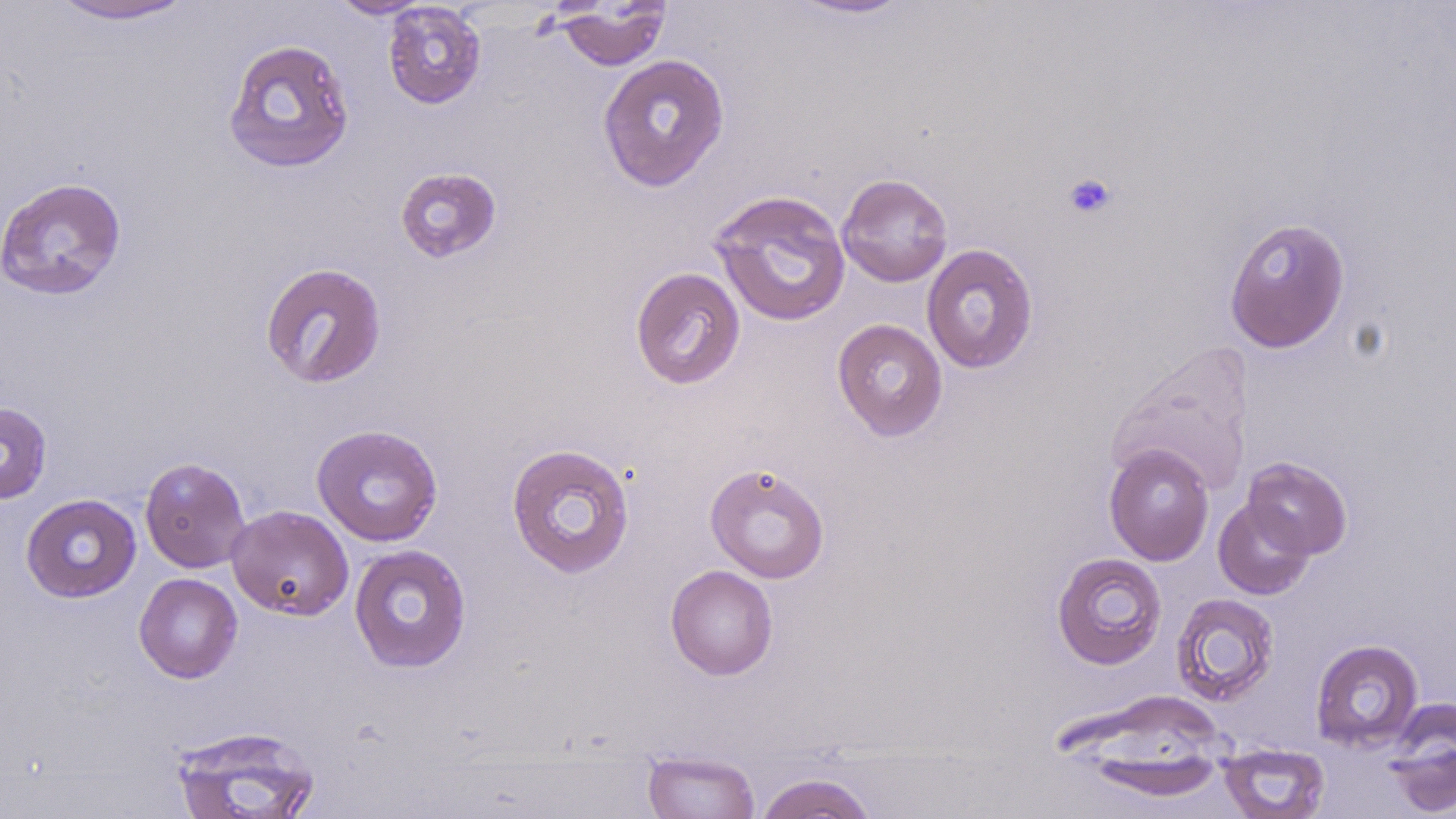

Summary:
  - Coordinate format: approximate bounding boxes as (x1,y1)-(x2,y2) corner pairs in pixels
  - Uninfected red blood cell locations: (46,0)-(199,24), (328,0)-(434,19), (784,0)-(917,20), (382,2)-(487,110), (554,2)-(672,71), (222,38)-(356,174), (597,53)-(730,192), (394,167)-(502,263), (836,172)-(953,287), (0,176)-(128,300), (710,189)-(851,327), (1223,216)-(1351,353), (921,243)-(1038,374), (259,262)-(387,388), (630,266)-(746,390), (832,318)-(948,441), (1108,342)-(1255,497), (0,401)-(52,504), (311,424)-(443,546), (505,443)-(636,578), (1104,445)-(1214,566), (139,456)-(251,573), (1242,457)-(1352,559), (704,462)-(830,583), (20,493)-(141,603), (1213,498)-(1315,600), (226,504)-(354,620), (349,543)-(472,673), (1051,552)-(1167,670), (665,564)-(778,680), (134,573)-(243,683), (1170,592)-(1279,706), (1310,638)-(1424,753), (1384,702)-(1456,817), (169,724)-(322,818), (1218,742)-(1330,819), (643,750)-(760,819), (1077,752)-(1227,802), (754,772)-(879,819)
  - Platelet locations: (1062,172)-(1117,220)
  - Slide-level diagnosis: no evidence of blood parasites
  - Stain: May-Grünwald-Giemsa
  - Preparation: thin blood smear
  - Field of view: single
  - Modality: light microscopy
  - Image size: 1456×819 pixels
  - Magnification: 1000x